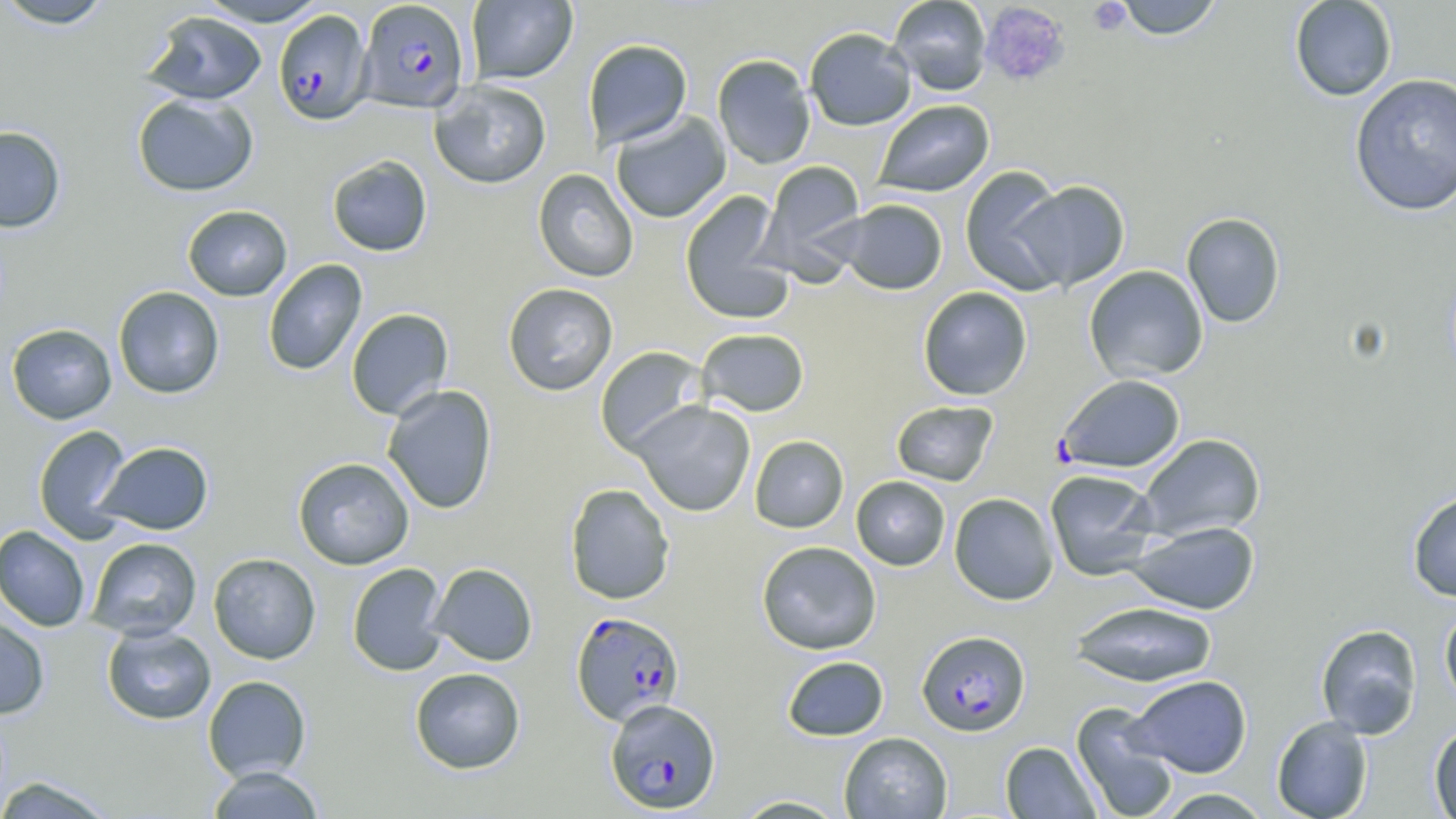

Summary:
  - Coordinate format: approximate bounding boxes as named x1/y1/x2/y2 corners in pixels
  - Platelet locations: (x1=1088, y1=1, x2=1132, y2=35), (x1=980, y1=2, x2=1072, y2=89)
  - Uninfected red blood cell locations: (x1=0, y1=0, x2=116, y2=29), (x1=195, y1=0, x2=330, y2=27), (x1=466, y1=0, x2=577, y2=84), (x1=887, y1=0, x2=992, y2=96), (x1=1114, y1=0, x2=1225, y2=40), (x1=1289, y1=0, x2=1398, y2=101), (x1=141, y1=10, x2=267, y2=105), (x1=804, y1=27, x2=916, y2=131), (x1=583, y1=39, x2=693, y2=150), (x1=712, y1=54, x2=816, y2=170), (x1=1349, y1=73, x2=1456, y2=217), (x1=429, y1=80, x2=551, y2=189), (x1=131, y1=92, x2=259, y2=197), (x1=873, y1=100, x2=994, y2=198), (x1=610, y1=112, x2=731, y2=223), (x1=0, y1=125, x2=66, y2=232), (x1=326, y1=154, x2=433, y2=257), (x1=759, y1=159, x2=868, y2=274), (x1=960, y1=166, x2=1071, y2=295), (x1=533, y1=168, x2=639, y2=282), (x1=1012, y1=180, x2=1130, y2=291), (x1=679, y1=191, x2=794, y2=324), (x1=836, y1=199, x2=947, y2=295), (x1=182, y1=205, x2=292, y2=301), (x1=1181, y1=212, x2=1286, y2=328), (x1=262, y1=259, x2=367, y2=376), (x1=1084, y1=265, x2=1208, y2=382), (x1=502, y1=283, x2=618, y2=395), (x1=113, y1=286, x2=225, y2=398), (x1=918, y1=286, x2=1032, y2=401), (x1=346, y1=308, x2=454, y2=420), (x1=6, y1=323, x2=117, y2=424), (x1=696, y1=328, x2=810, y2=417), (x1=594, y1=346, x2=709, y2=456), (x1=382, y1=385, x2=498, y2=515), (x1=890, y1=400, x2=999, y2=486), (x1=631, y1=401, x2=755, y2=517), (x1=33, y1=425, x2=133, y2=544), (x1=1137, y1=434, x2=1266, y2=541), (x1=749, y1=435, x2=849, y2=533), (x1=94, y1=441, x2=214, y2=535), (x1=292, y1=457, x2=414, y2=570), (x1=1045, y1=469, x2=1160, y2=580), (x1=851, y1=476, x2=951, y2=571), (x1=564, y1=483, x2=675, y2=605), (x1=1407, y1=489, x2=1456, y2=602), (x1=948, y1=492, x2=1059, y2=605), (x1=1126, y1=520, x2=1261, y2=615), (x1=0, y1=525, x2=91, y2=632), (x1=86, y1=537, x2=202, y2=640), (x1=756, y1=540, x2=882, y2=655), (x1=208, y1=553, x2=321, y2=664), (x1=428, y1=562, x2=538, y2=666), (x1=347, y1=563, x2=448, y2=677), (x1=1069, y1=600, x2=1218, y2=687), (x1=1439, y1=604, x2=1456, y2=711), (x1=0, y1=613, x2=50, y2=720), (x1=101, y1=624, x2=217, y2=725), (x1=1315, y1=624, x2=1423, y2=740), (x1=781, y1=655, x2=889, y2=741), (x1=409, y1=667, x2=526, y2=774), (x1=1128, y1=674, x2=1253, y2=777), (x1=202, y1=675, x2=311, y2=782), (x1=1071, y1=701, x2=1180, y2=819), (x1=1271, y1=715, x2=1373, y2=819), (x1=1428, y1=723, x2=1456, y2=818), (x1=839, y1=732, x2=952, y2=819), (x1=1000, y1=741, x2=1101, y2=818), (x1=205, y1=765, x2=327, y2=819), (x1=0, y1=776, x2=121, y2=818), (x1=1153, y1=787, x2=1273, y2=818), (x1=729, y1=795, x2=851, y2=818)
  - Plasmodium falciparum-infected red blood cell locations: (x1=357, y1=0, x2=469, y2=113), (x1=273, y1=9, x2=373, y2=125), (x1=1056, y1=374, x2=1186, y2=474), (x1=571, y1=610, x2=685, y2=726), (x1=917, y1=630, x2=1030, y2=736), (x1=604, y1=697, x2=722, y2=814)
  - Slide-level diagnosis: Plasmodium falciparum
  - Field of view: single
  - Magnification: 1000x
  - Modality: light microscopy
  - Stain: May-Grünwald-Giemsa
  - Preparation: thin blood smear
  - Image size: 1456×819 pixels